State the blood parasite species.
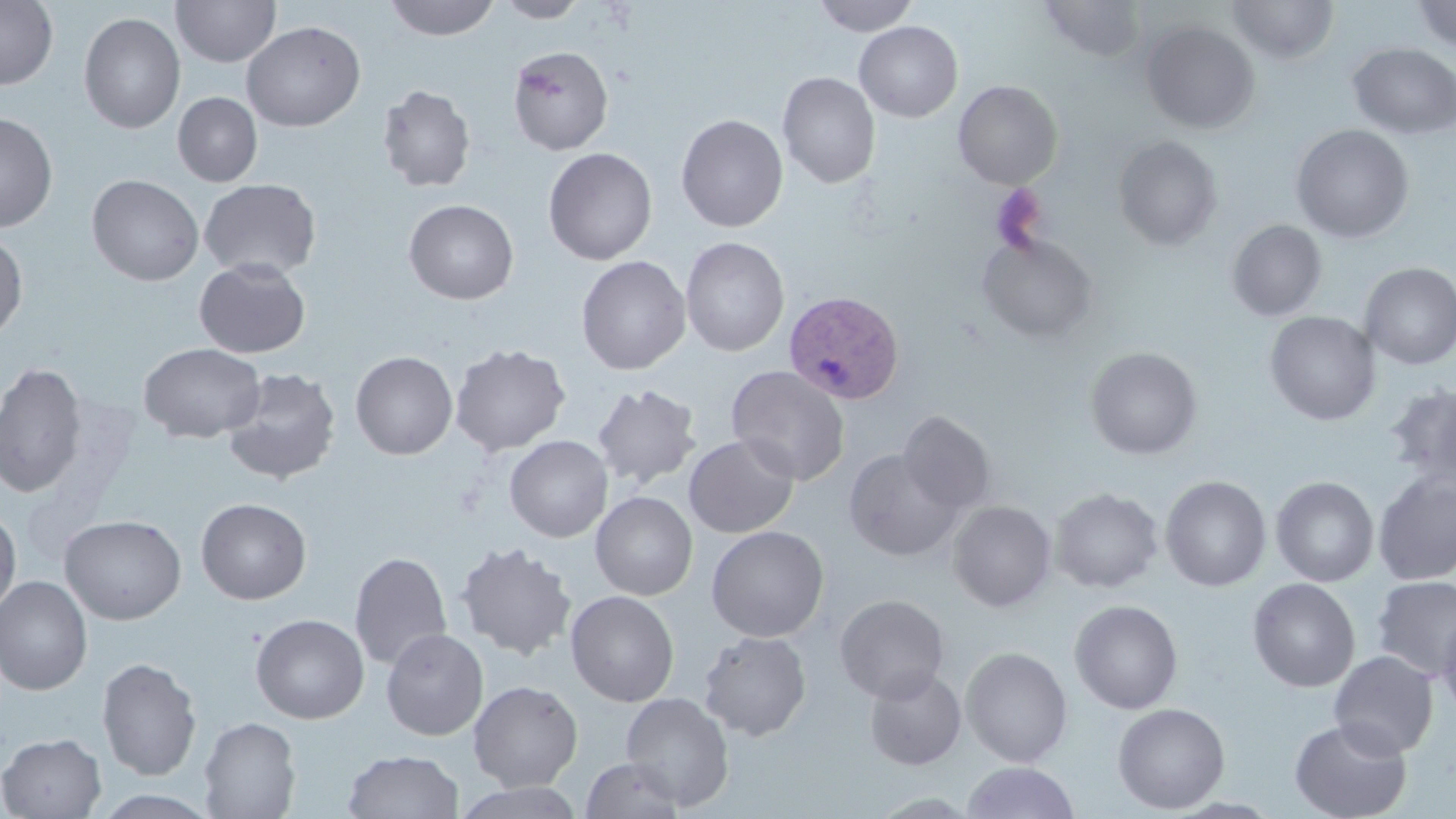

Plasmodium vivax.

stain = May-Grünwald-Giemsa
Plasmodium vivax-infected red blood cell locations = approximate bounding boxes as [x1, y1, x2, y2] in pixels: [782, 289, 906, 405]
modality = light microscopy
uninfected red blood cell locations = approximate bounding boxes as [x1, y1, x2, y2] in pixels: [382, 0, 501, 41], [495, 0, 590, 23], [811, 0, 920, 36], [1041, 0, 1148, 62], [1227, 0, 1339, 64], [1411, 0, 1456, 51], [0, 1, 58, 90], [171, 1, 281, 67], [78, 12, 185, 133], [242, 21, 366, 132], [854, 21, 963, 122], [1141, 21, 1260, 134], [1347, 43, 1456, 139], [508, 44, 614, 155], [777, 72, 880, 188], [953, 80, 1063, 189], [377, 84, 477, 192], [172, 92, 262, 187], [0, 113, 58, 232], [676, 114, 788, 232], [1291, 125, 1415, 244], [1113, 135, 1223, 250], [543, 147, 658, 265], [86, 174, 204, 285], [199, 178, 322, 280], [403, 199, 519, 304], [1226, 219, 1327, 322], [0, 230, 28, 342], [976, 235, 1100, 344], [679, 236, 789, 356], [576, 255, 691, 374], [194, 258, 311, 359], [1359, 263, 1456, 370], [1264, 311, 1381, 426], [138, 342, 266, 443], [450, 343, 571, 456], [1085, 347, 1202, 460], [350, 351, 458, 460], [0, 360, 87, 498], [726, 365, 850, 486], [221, 367, 341, 486], [591, 382, 702, 489], [1386, 384, 1456, 490], [898, 410, 996, 514], [684, 433, 799, 538], [504, 435, 612, 542], [843, 449, 963, 562], [1373, 473, 1456, 584], [1160, 476, 1271, 591], [1271, 477, 1379, 587], [1050, 487, 1163, 593], [590, 492, 698, 601], [195, 498, 312, 604], [947, 500, 1057, 612], [0, 506, 21, 617], [60, 514, 187, 625], [706, 526, 829, 643], [455, 541, 577, 660], [349, 551, 452, 671], [1372, 575, 1456, 681], [0, 576, 93, 696], [1248, 578, 1360, 692], [565, 590, 680, 707], [834, 594, 950, 704], [1069, 600, 1183, 714], [1438, 609, 1456, 722], [250, 614, 369, 724], [381, 628, 488, 741], [698, 631, 811, 742], [961, 646, 1072, 768], [1328, 650, 1439, 759], [97, 657, 202, 780], [863, 668, 967, 770], [468, 680, 583, 791], [620, 692, 735, 810], [1113, 703, 1230, 814], [199, 716, 301, 818], [1288, 718, 1412, 819], [0, 733, 107, 818], [343, 749, 464, 818], [580, 757, 686, 819], [960, 762, 1081, 819], [453, 782, 586, 819]
magnification = 1000x
image size = 1456×819 pixels
preparation = thin blood smear
field of view = single
platelet locations = approximate bounding boxes as [x1, y1, x2, y2] in pixels: [990, 184, 1049, 253]